Comment on the morphology of the erythrocytes.
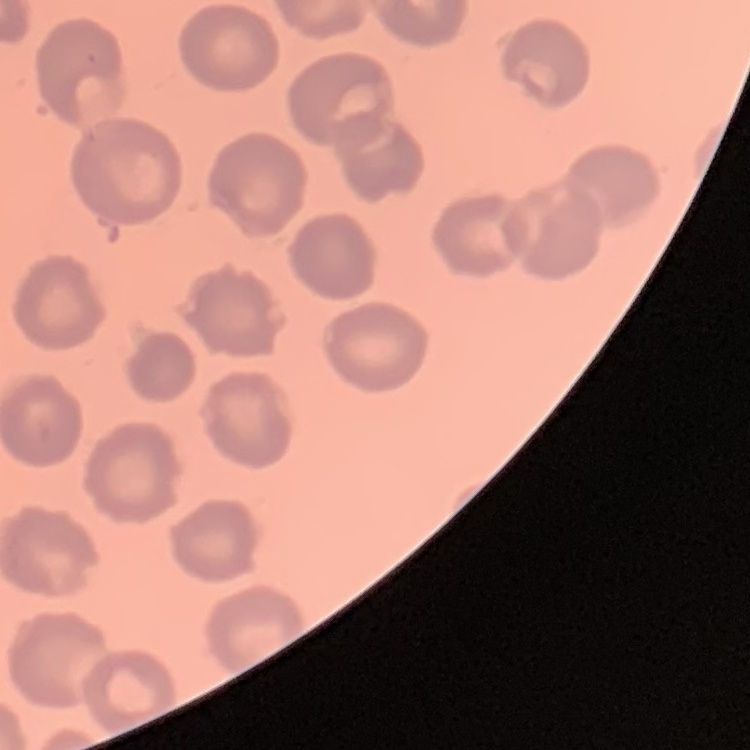
No rouleaux formation.

Stained with either Field's or Giemsa. Square crop of a larger photomicrograph. Thin blood film.